Locate every uninfected red blood cell.
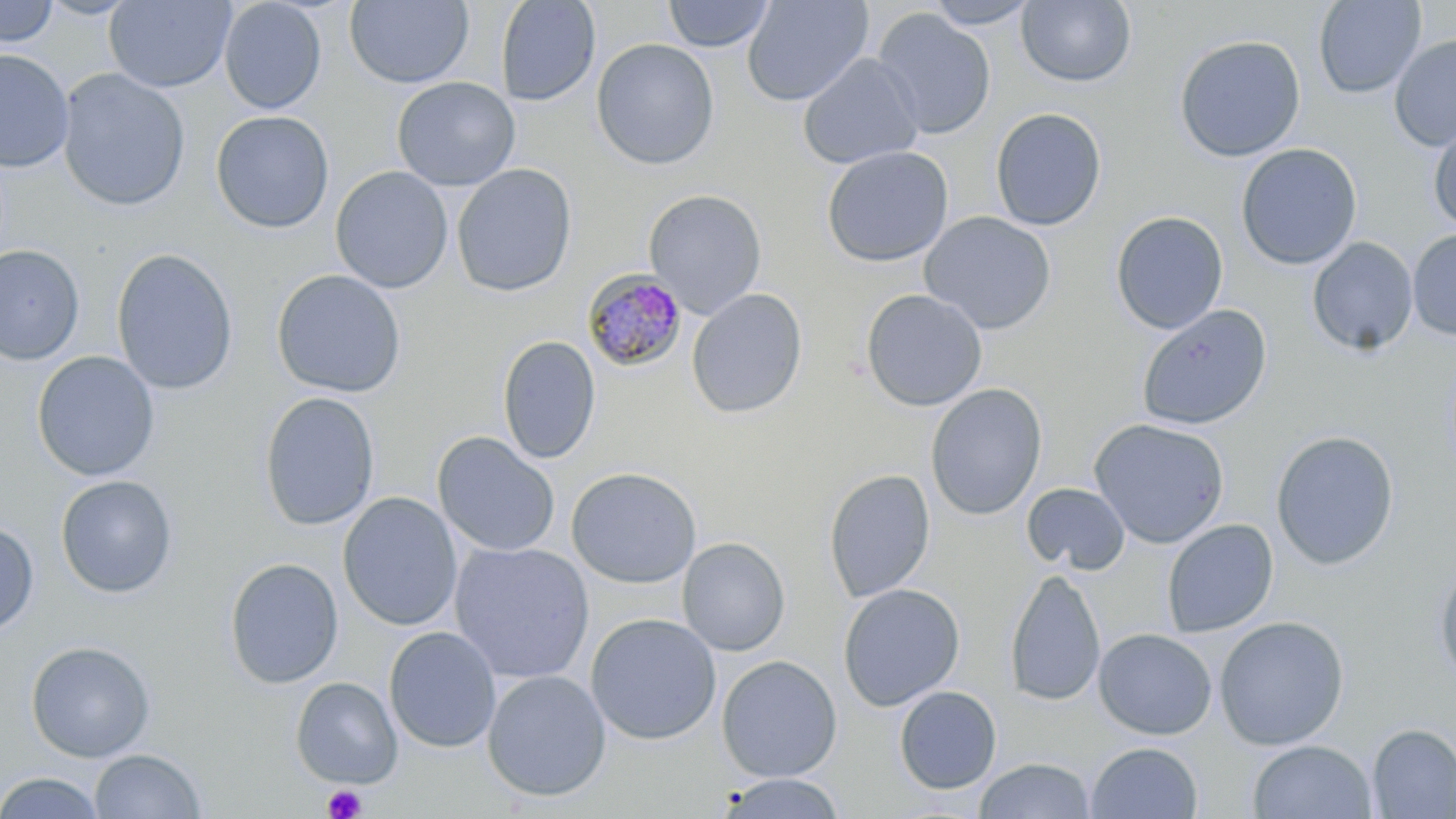
Approximate bounding boxes as named x1/y1/x2/y2 corners in pixels.
Uninfected red blood cells (subset): (x1=104, y1=0, x2=236, y2=92), (x1=218, y1=0, x2=327, y2=115), (x1=345, y1=0, x2=474, y2=88), (x1=495, y1=0, x2=601, y2=107), (x1=662, y1=0, x2=776, y2=53), (x1=741, y1=0, x2=873, y2=107), (x1=1312, y1=0, x2=1426, y2=99), (x1=0, y1=1, x2=59, y2=47), (x1=922, y1=1, x2=1041, y2=29), (x1=1016, y1=1, x2=1136, y2=88), (x1=871, y1=8, x2=996, y2=140), (x1=1174, y1=34, x2=1306, y2=162), (x1=1389, y1=34, x2=1456, y2=153), (x1=591, y1=38, x2=720, y2=170), (x1=0, y1=49, x2=74, y2=172), (x1=797, y1=53, x2=924, y2=170), (x1=57, y1=68, x2=191, y2=212), (x1=392, y1=76, x2=520, y2=191), (x1=990, y1=107, x2=1107, y2=231), (x1=210, y1=110, x2=334, y2=233), (x1=1427, y1=121, x2=1456, y2=234), (x1=1236, y1=143, x2=1362, y2=270), (x1=820, y1=145, x2=954, y2=267), (x1=451, y1=163, x2=577, y2=297), (x1=331, y1=166, x2=453, y2=293), (x1=643, y1=188, x2=767, y2=319), (x1=919, y1=211, x2=1057, y2=335), (x1=1110, y1=211, x2=1229, y2=335), (x1=1407, y1=229, x2=1456, y2=341), (x1=1306, y1=236, x2=1419, y2=356), (x1=0, y1=244, x2=84, y2=365), (x1=111, y1=247, x2=238, y2=396), (x1=271, y1=269, x2=407, y2=397), (x1=686, y1=287, x2=807, y2=419), (x1=860, y1=288, x2=988, y2=411), (x1=1136, y1=304, x2=1273, y2=431), (x1=497, y1=335, x2=601, y2=465), (x1=32, y1=350, x2=160, y2=481), (x1=925, y1=383, x2=1048, y2=521), (x1=259, y1=391, x2=380, y2=531), (x1=1089, y1=418, x2=1230, y2=549), (x1=1270, y1=430, x2=1399, y2=570), (x1=432, y1=431, x2=561, y2=558), (x1=566, y1=467, x2=702, y2=589), (x1=824, y1=469, x2=935, y2=603), (x1=55, y1=475, x2=177, y2=598), (x1=1022, y1=483, x2=1130, y2=575), (x1=338, y1=492, x2=463, y2=632), (x1=1162, y1=518, x2=1279, y2=637), (x1=0, y1=521, x2=39, y2=636), (x1=677, y1=536, x2=790, y2=656), (x1=449, y1=541, x2=596, y2=684), (x1=224, y1=557, x2=344, y2=689), (x1=1433, y1=564, x2=1456, y2=686), (x1=1004, y1=568, x2=1106, y2=707), (x1=837, y1=582, x2=965, y2=712), (x1=585, y1=613, x2=722, y2=745), (x1=1214, y1=616, x2=1349, y2=750), (x1=383, y1=625, x2=502, y2=753), (x1=1093, y1=627, x2=1217, y2=739), (x1=25, y1=641, x2=156, y2=762), (x1=716, y1=655, x2=842, y2=782), (x1=482, y1=670, x2=611, y2=802), (x1=290, y1=677, x2=402, y2=789), (x1=894, y1=685, x2=1002, y2=795), (x1=1367, y1=723, x2=1456, y2=818), (x1=1247, y1=739, x2=1377, y2=818), (x1=1086, y1=741, x2=1203, y2=818), (x1=89, y1=748, x2=206, y2=818), (x1=974, y1=758, x2=1095, y2=819), (x1=0, y1=771, x2=106, y2=819), (x1=715, y1=772, x2=848, y2=818).

Summary:
  - Platelet locations: (x1=322, y1=784, x2=367, y2=819)
  - Slide-level diagnosis: Plasmodium malariae
  - Modality: light microscopy
  - Magnification: 1000x
  - Stain: May-Grünwald-Giemsa
  - Preparation: thin blood smear
  - Field of view: single
  - Image size: 1456×819 pixels